Locate Plasmodium parasites and leukocytes.
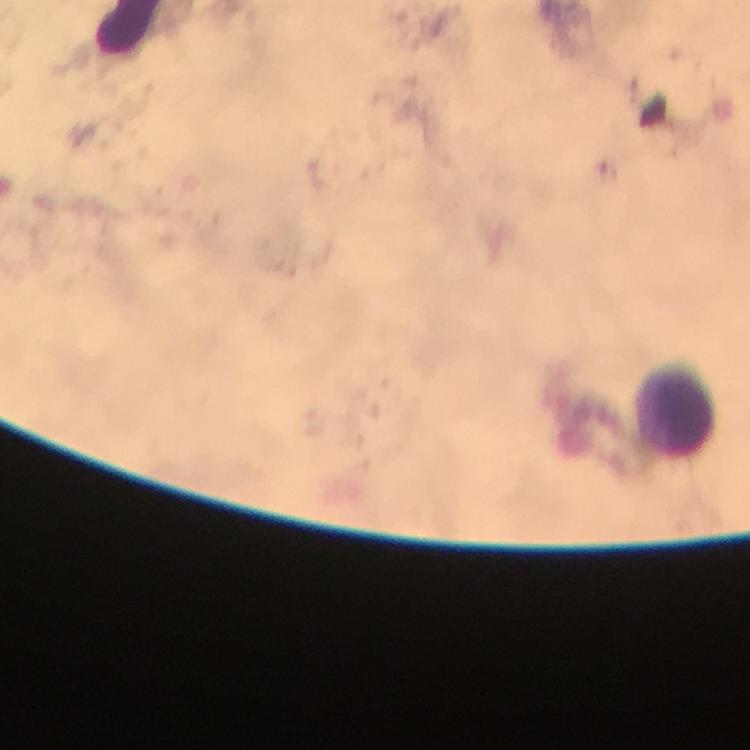
No Plasmodium parasites seen.
Approximate centers as (x, y) in pixels.
Leukocytes: (674, 419).

immersion oil = applied
image size = 750×750 pixels
capture = smartphone camera through the microscope
stain = Giemsa
preparation = thick blood film
magnification = 100x
context = from a malaria diagnostic workup
cropped from = a single field of view